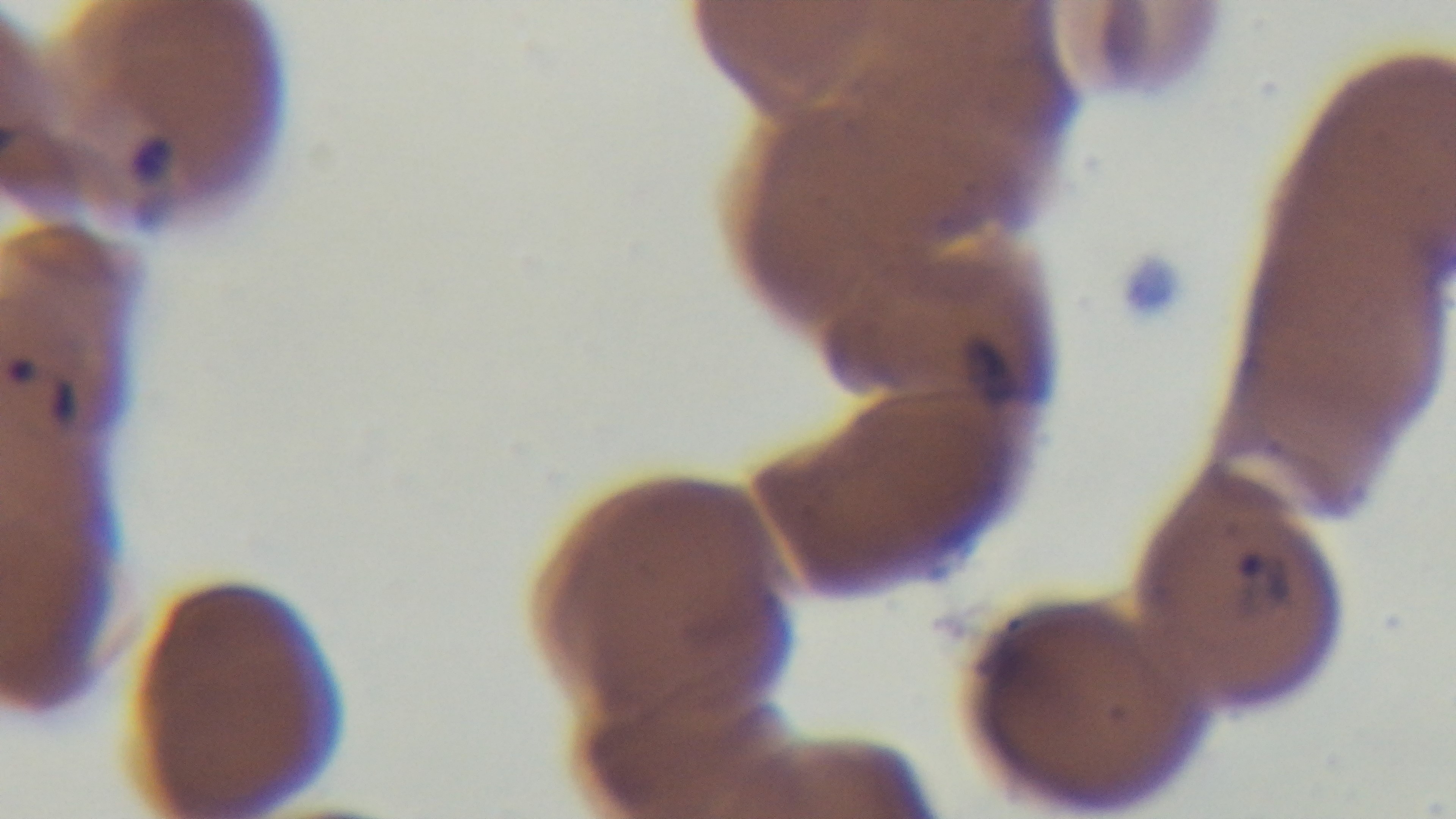

Malaria status: infected. Preparation: thin smear. Captured with a mounted 4K digital camera. Giemsa stain. One field from the slide. 100x oil-immersion objective. Light microscopy.